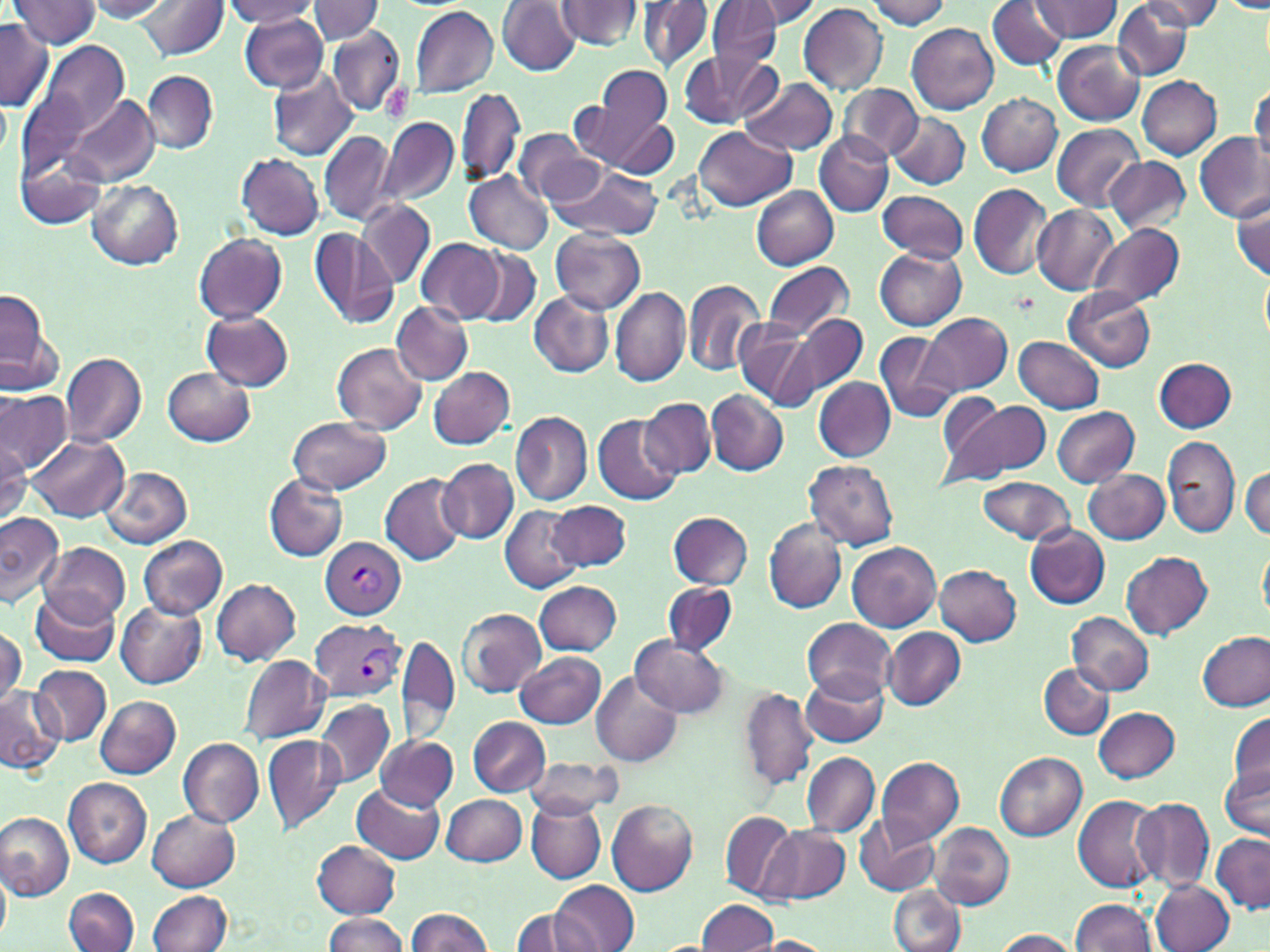

slide_level_diagnosis: Plasmodium vivax
image_size: 1270×952 pixels
plasmodium_vivax_infected_red_blood_cell_locations: 'approximate bounding boxes as (x1,y1)-(x2,y2) corner pairs in pixels: (320,536)-(406,620), (312,619)-(404,702)'
stain: May-Grünwald-Giemsa
modality: light microscopy
platelet_locations: 'approximate bounding boxes as (x1,y1)-(x2,y2) corner pairs in pixels: (380,84)-(409,119)'
field_of_view: single
preparation: thin blood smear
uninfected_red_blood_cell_locations: 'approximate bounding boxes as (x1,y1)-(x2,y2) corner pairs in pixels: (10,0)-(102,50), (87,0)-(175,21), (224,0)-(321,27), (309,0)-(384,43), (497,0)-(583,76), (557,0)-(642,51), (987,0)-(1066,71), (1033,0)-(1122,42), (1140,0)-(1225,30), (139,1)-(227,61), (637,1)-(713,71), (734,1)-(821,34), (863,1)-(951,28), (706,2)-(785,68), (1111,2)-(1193,79), (799,3)-(887,94), (1221,3)-(1270,12), (408,5)-(500,99), (238,13)-(328,92), (250,15)-(341,157), (0,18)-(53,112), (907,21)-(1000,114), (326,25)-(404,117), (1052,41)-(1144,125), (26,42)-(129,147), (677,53)-(774,129), (582,66)-(676,167), (267,69)-(357,162), (144,71)-(218,153), (738,75)-(838,156), (1137,75)-(1222,160), (1249,82)-(1269,169), (839,84)-(923,159), (455,86)-(524,185), (64,92)-(159,187), (977,92)-(1062,176), (888,111)-(971,191), (606,117)-(680,177), (378,118)-(459,208), (1051,123)-(1146,210), (693,124)-(795,210), (512,129)-(603,207), (319,130)-(397,227), (815,132)-(892,216), (1194,132)-(1268,223), (18,151)-(106,229), (235,153)-(324,239), (1105,157)-(1193,234), (547,164)-(664,241), (464,170)-(554,254), (87,180)-(183,269), (969,183)-(1053,280), (751,184)-(839,268), (876,190)-(970,263), (1231,192)-(1270,283), (357,200)-(435,289), (1033,206)-(1117,295), (1091,223)-(1185,306), (310,229)-(399,330), (551,229)-(645,312), (194,233)-(287,323), (416,238)-(504,322), (471,247)-(541,326), (875,249)-(967,330), (762,262)-(853,339), (1260,269)-(1269,349), (682,277)-(766,376), (609,287)-(689,387), (1064,287)-(1157,372), (0,288)-(53,381), (530,292)-(613,377), (392,302)-(472,385), (202,311)-(294,390), (921,311)-(1011,395), (786,313)-(867,398), (733,318)-(819,410), (874,331)-(958,423), (1012,335)-(1105,413), (331,342)-(427,435), (60,352)-(147,448), (1154,358)-(1236,433), (164,366)-(256,446), (427,367)-(514,449), (812,377)-(896,461), (707,390)-(787,474), (0,392)-(73,474), (938,396)-(1049,486), (640,397)-(716,477), (1052,407)-(1139,486), (510,411)-(592,504), (592,413)-(681,504), (289,416)-(391,494), (27,434)-(129,521), (1163,434)-(1240,539), (0,440)-(31,525), (438,458)-(518,544), (804,460)-(899,551), (100,466)-(194,547), (1241,467)-(1270,539), (1084,469)-(1169,544), (264,473)-(348,562), (379,473)-(469,564), (977,477)-(1074,544), (549,501)-(631,571), (500,505)-(585,593), (0,511)-(64,607), (667,511)-(754,590), (764,518)-(846,614), (1025,524)-(1111,609), (137,536)-(228,618), (1258,539)-(1269,625), (847,541)-(942,630), (41,543)-(131,627), (1121,551)-(1213,639), (935,564)-(1021,645), (211,577)-(301,665), (534,579)-(621,655), (662,581)-(738,655), (30,591)-(119,666), (116,601)-(207,688), (457,608)-(545,697), (1069,612)-(1154,695), (803,617)-(895,701), (0,627)-(25,711), (884,628)-(966,709), (397,633)-(460,745), (1199,633)-(1269,710), (630,635)-(727,718), (515,652)-(605,728), (240,654)-(332,743), (1040,663)-(1113,738), (31,664)-(113,744), (803,671)-(888,749), (591,673)-(682,768), (0,686)-(64,769), (739,688)-(818,789), (95,695)-(181,779), (289,698)-(394,846), (316,698)-(394,786), (1093,706)-(1179,783), (1228,711)-(1270,795), (467,717)-(551,796), (263,732)-(345,832), (376,734)-(458,810), (177,736)-(263,828), (803,752)-(879,838), (995,752)-(1086,842), (524,757)-(623,817), (875,757)-(963,845), (1221,762)-(1269,840), (62,778)-(151,869), (352,783)-(446,864), (1073,794)-(1165,894), (441,795)-(528,865), (1132,796)-(1215,893), (525,798)-(605,882), (606,799)-(699,896), (148,809)-(240,891), (0,812)-(73,899), (721,812)-(794,899), (854,815)-(940,896), (930,822)-(1014,910), (761,826)-(850,905), (1211,833)-(1270,914), (312,840)-(401,919), (0,871)-(10,943), (1152,879)-(1234,952), (549,882)-(638,951), (889,883)-(966,952), (65,888)-(139,952), (149,891)-(232,952), (697,899)-(778,950), (1071,899)-(1158,952), (405,907)-(496,952), (510,908)-(592,952), (322,913)-(408,951), (992,929)-(1079,951), (756,936)-(834,951)'
magnification: 1000x